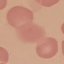
Summary:
  - Malaria status: uninfected
  - Capture: smartphone camera at the microscope eyepiece
  - Preparation: thin smear
  - Stain: Giemsa
  - Image type: automatically extracted cell patch, resized to 64 × 64 pixels